Describe the morphology of the erythrocytes.
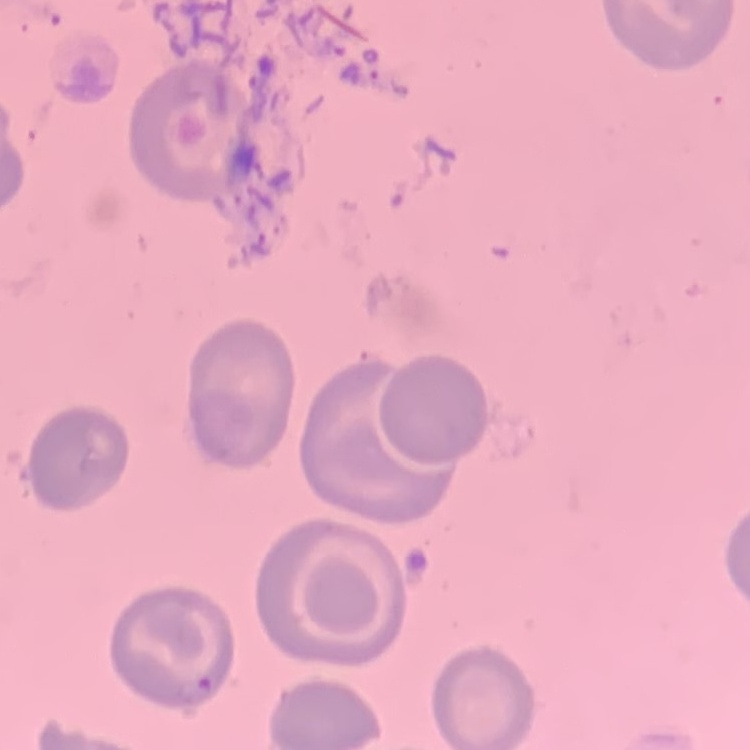

No rouleaux formation.

Stained with either Field's or Giemsa. One tile cut from a larger photomicrograph. Thin blood smear.